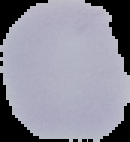
image type = cell region segmented out of the field of view; surrounding area masked to black
preparation = thin blood smear
result = malaria parasites identified
image size = 130×142 pixels